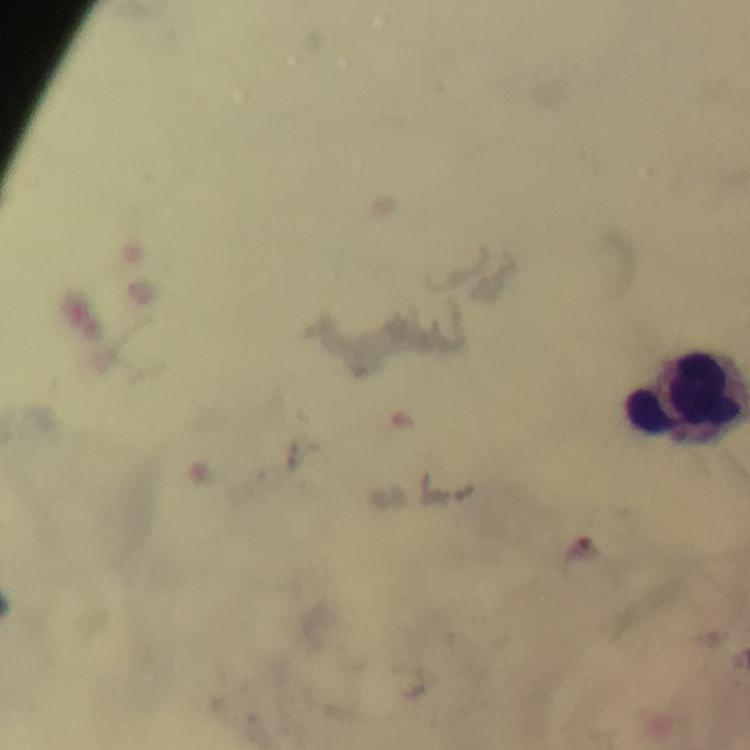
{
  "magnification": "100x",
  "plasmodium_parasite_locations": "approximate object centers, in pixels from the top-left corner: (x=582, y=547)",
  "leukocyte_locations": "approximate object centers, in pixels from the top-left corner: (x=687, y=399)",
  "immersion_oil": "applied",
  "cropped_from": "a single field of view",
  "stain": "Giemsa",
  "capture": "smartphone mounted on the microscope",
  "image_size": "750×750 pixels",
  "context": "from a malaria diagnostic workup",
  "preparation": "thick blood smear"
}